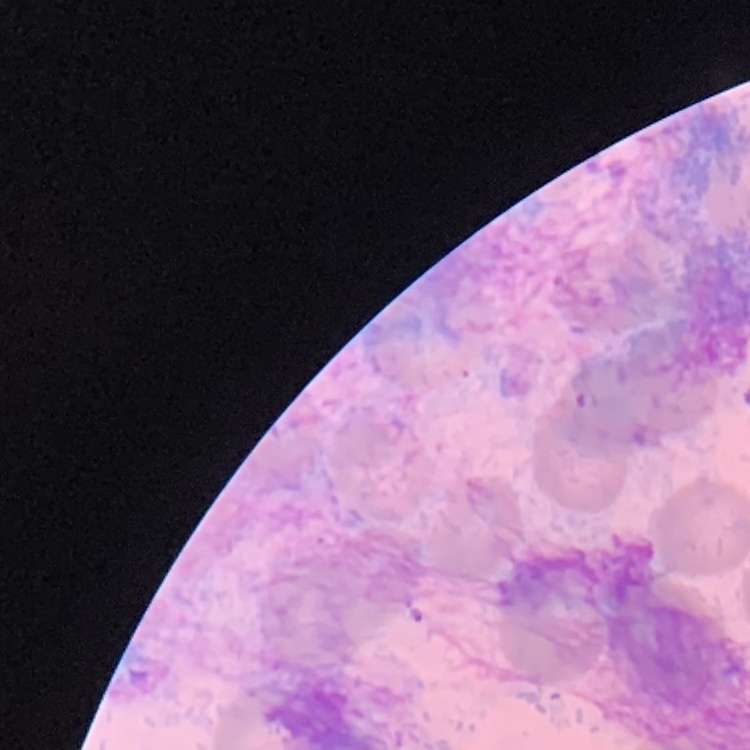
{
  "erythrocyte_morphology": "no rouleaux formation",
  "image_type": "one tile cut from a larger photomicrograph",
  "stain": "Field's or Giemsa",
  "preparation": "thin blood smear"
}